Name the parasite shown.
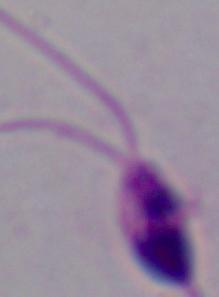

Leishmania.

Captured at 1000x magnification. Micrograph.